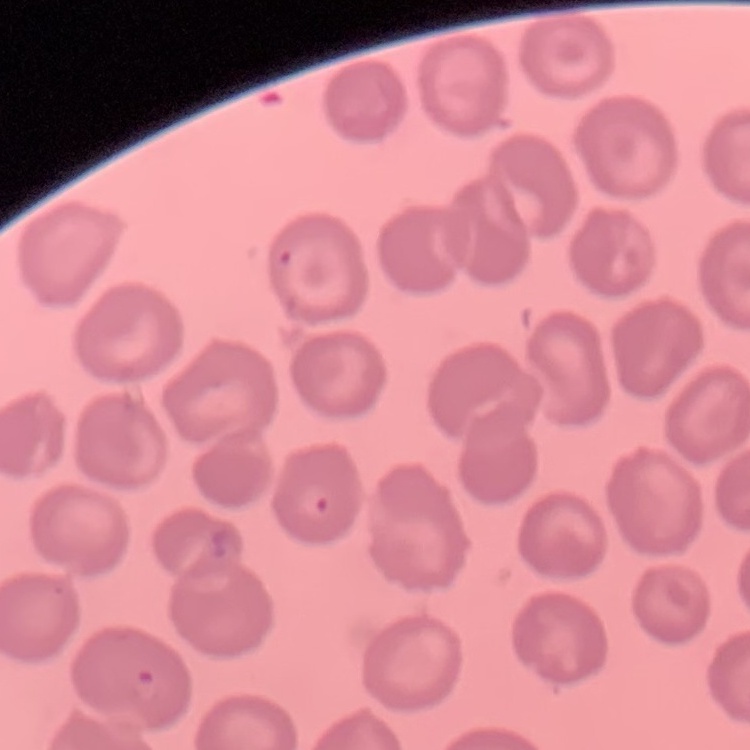

red blood cell morphology = no rouleaux formation
image type = square crop of a larger photomicrograph
stain = Field's or Giemsa
preparation = thin peripheral smear